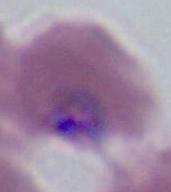
Summary:
  - Magnification: 400x or 1000x
  - Modality: photomicrograph
  - Identification: Plasmodium